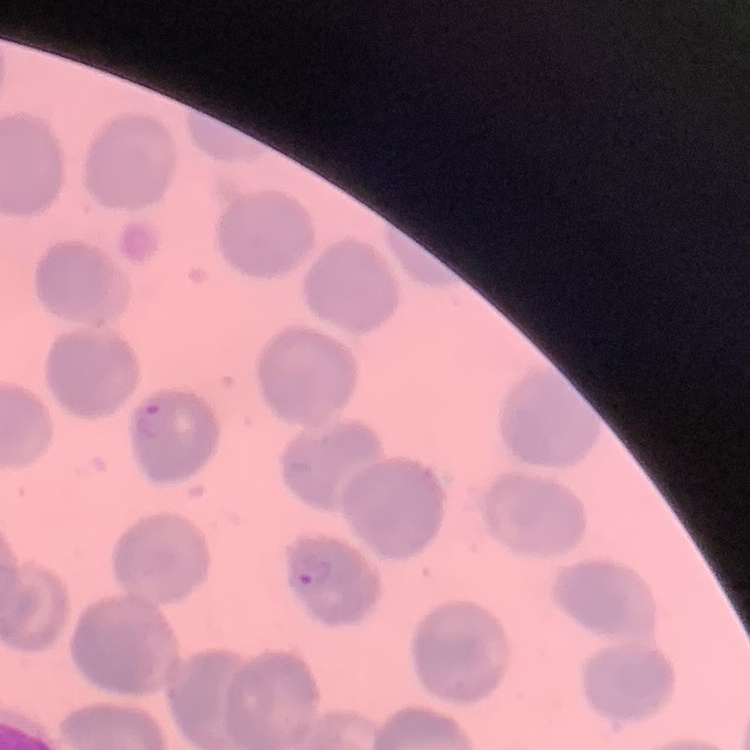 The red blood cells exhibit no rouleaux formation. Thin blood film. Stained with either Field's or Giemsa. Square crop of a larger photomicrograph.